Name the parasite shown.
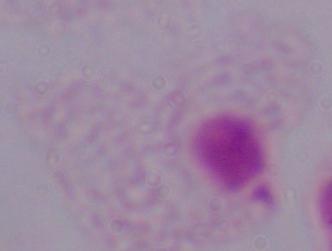

This is a trichomonad.

Photomicrograph. Captured at 1000x magnification.